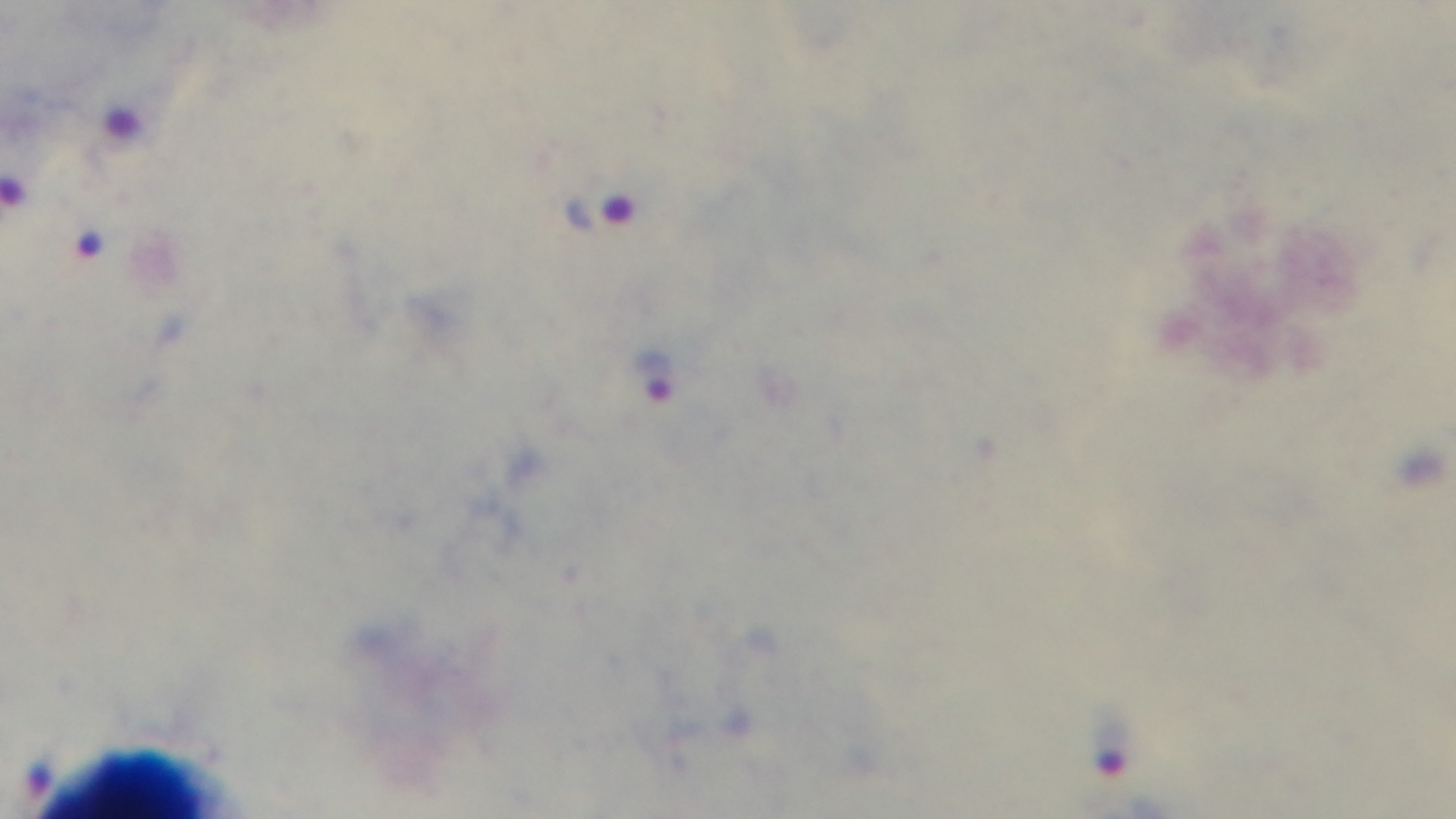
Summary:
  - Field of view: one from the slide
  - Malaria status: infected
  - Capture: mounted 4K digital camera
  - Preparation: thick
  - Stain: Giemsa
  - Objective: 100x oil immersion
  - Modality: light microscopy